Locate every Plasmodium malariae-infected red blood cell.
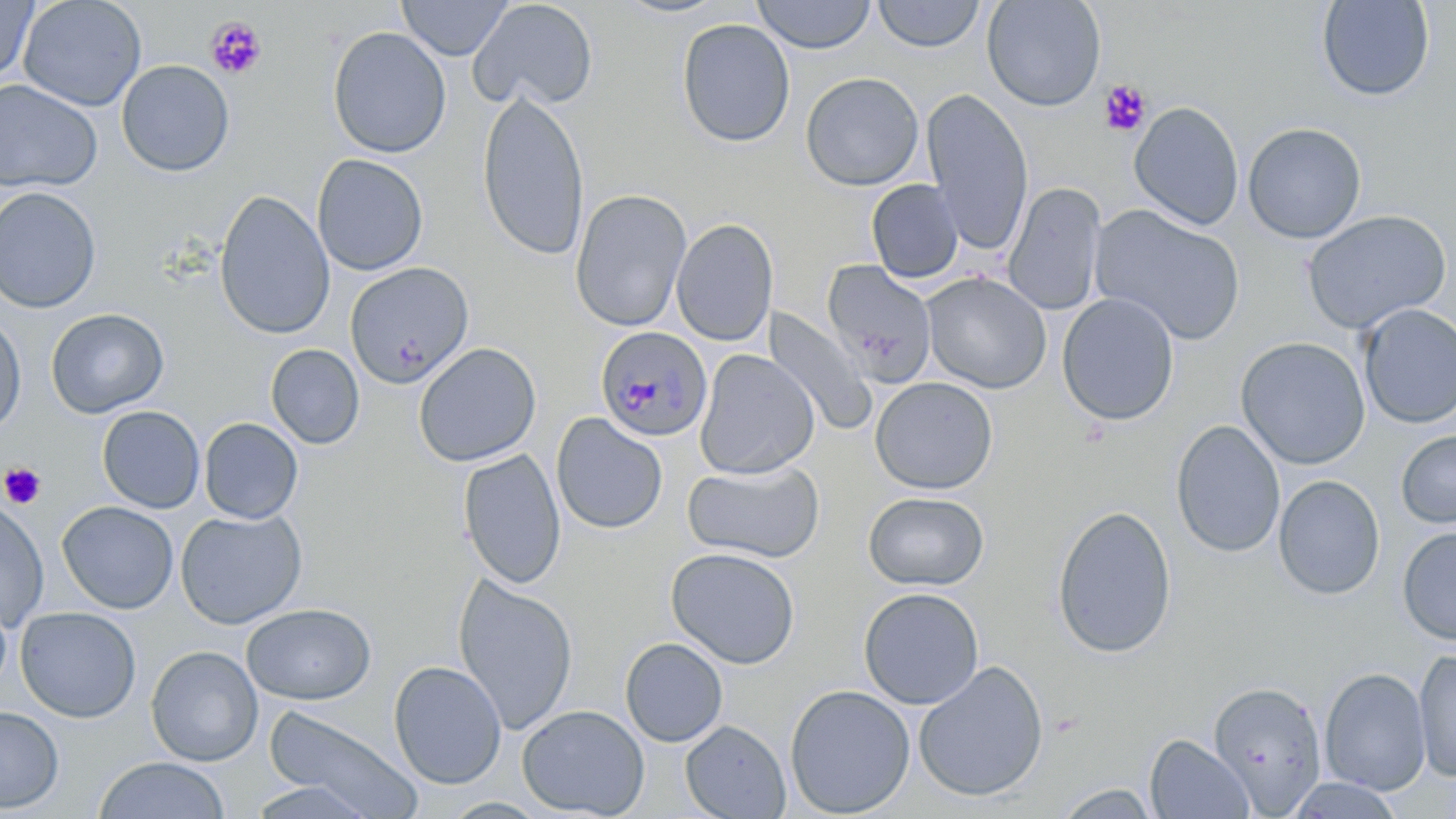

Approximate bounding boxes as [x1, y1, x2, y2] in pixels.
Plasmodium malariae-infected red blood cells: [595, 325, 713, 441].

slide-level diagnosis = Plasmodium malariae
platelet locations = approximate bounding boxes as [x1, y1, x2, y2] in pixels: [205, 16, 267, 79], [1099, 79, 1152, 137], [1, 462, 46, 509]
image size = 1456×819 pixels
field of view = one of a larger specimen
preparation = thin blood smear
uninfected red blood cell locations = approximate bounding boxes as [x1, y1, x2, y2] in pixels: [17, 0, 147, 111], [398, 0, 512, 60], [468, 0, 599, 112], [613, 0, 731, 19], [752, 0, 876, 54], [982, 0, 1106, 111], [1316, 0, 1435, 102], [0, 1, 38, 83], [871, 1, 986, 53], [676, 18, 795, 148], [327, 26, 451, 159], [116, 60, 235, 177], [800, 71, 924, 191], [0, 78, 102, 193], [477, 88, 590, 261], [921, 88, 1034, 255], [1129, 101, 1244, 231], [1242, 122, 1367, 243], [311, 153, 429, 276], [866, 179, 964, 284], [1003, 182, 1106, 316], [0, 186, 102, 313], [214, 189, 335, 341], [570, 189, 691, 332], [1090, 205, 1246, 346], [1300, 210, 1452, 334], [672, 218, 778, 347], [821, 259, 938, 388], [344, 262, 474, 388], [921, 271, 1052, 394], [1056, 292, 1180, 426], [1356, 304, 1456, 430], [45, 308, 169, 418], [765, 308, 878, 437], [0, 313, 27, 435], [1235, 336, 1371, 470], [413, 342, 541, 467], [266, 344, 365, 449], [695, 348, 820, 480], [869, 376, 999, 495], [97, 406, 205, 513], [551, 413, 668, 534], [199, 417, 303, 524], [1171, 420, 1286, 558], [1396, 430, 1456, 528], [458, 449, 567, 589], [683, 460, 825, 563], [1273, 475, 1385, 600], [863, 492, 989, 590], [0, 498, 49, 632], [57, 501, 179, 613], [1050, 504, 1177, 659], [175, 509, 307, 628], [1397, 526, 1456, 646], [665, 547, 801, 669], [452, 574, 577, 735], [858, 588, 984, 709], [0, 597, 12, 697], [241, 602, 376, 704], [15, 606, 141, 722], [620, 637, 728, 747], [146, 645, 263, 766], [1413, 648, 1456, 783], [388, 660, 507, 789], [913, 661, 1049, 802], [1320, 666, 1431, 796], [1207, 680, 1328, 813], [784, 683, 916, 818], [517, 704, 650, 818], [0, 705, 64, 813], [262, 707, 423, 818], [680, 719, 790, 819], [1145, 734, 1254, 819], [94, 756, 230, 819], [1283, 777, 1405, 818], [242, 779, 386, 819], [1050, 784, 1163, 819]
magnification = 1000x
stain = May-Grünwald-Giemsa
modality = light microscopy